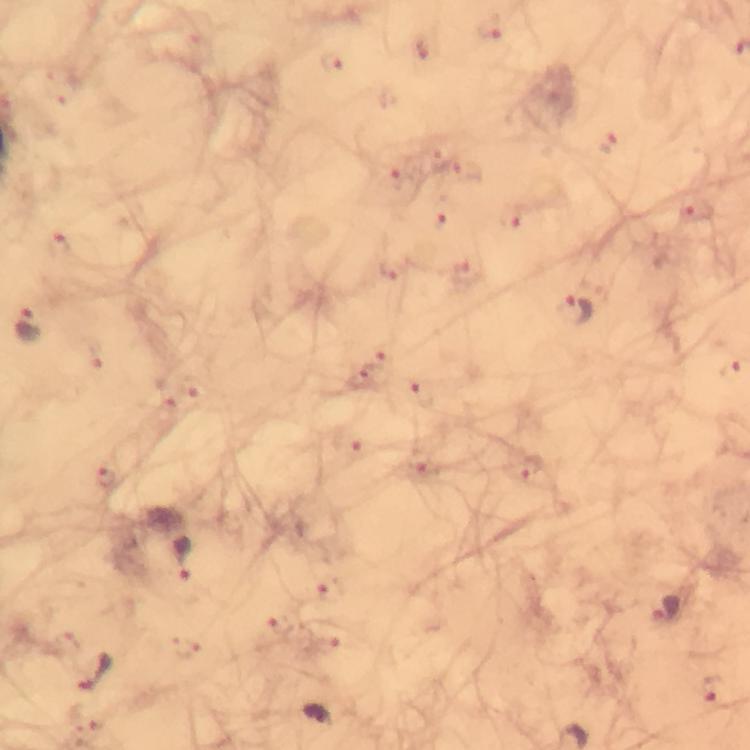
Approximate centers as (x, y) in pixels.
Summary:
  - Malaria parasite locations: (577, 312), (27, 326), (183, 560), (665, 610), (93, 673), (319, 716)
  - Immersion oil: used
  - Capture: smartphone camera through the microscope
  - Context: from a diagnostic examination for malaria
  - Preparation: thick blood smear
  - Cropped from: a single field of view
  - Stain: Giemsa
  - Magnification: 100x
  - Image size: 750×750 pixels